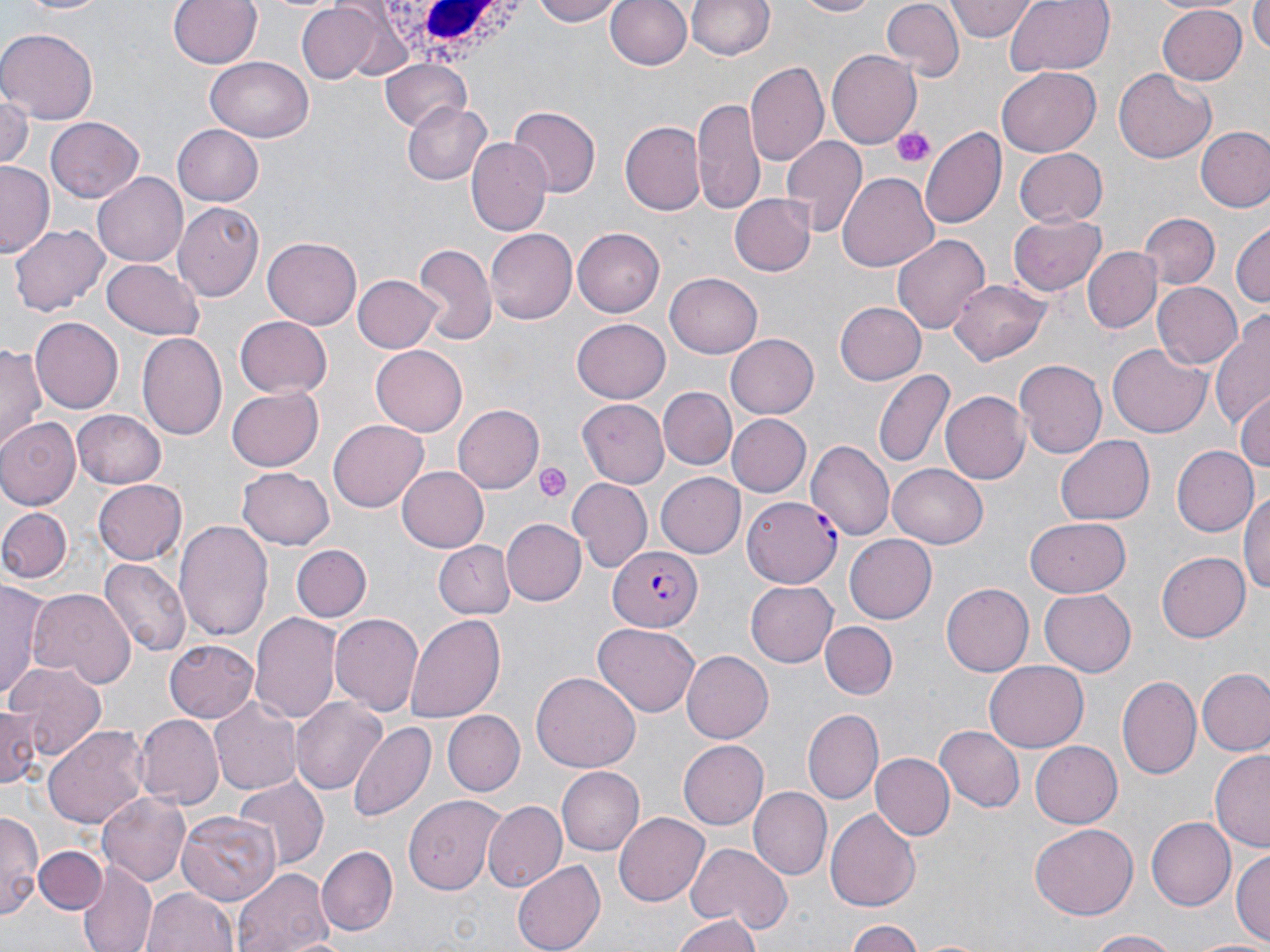
Approximate bounding boxes as (x1,y1)-(x2,y2) corner pairs in pixels. Platelet locations: (892,126)-(934,170), (534,462)-(571,502). White blood cell locations: (374,4)-(533,74). Uninfected red blood cell locations: (12,0)-(108,17), (168,0)-(261,70), (530,0)-(628,26), (606,0)-(691,72), (685,0)-(776,62), (793,0)-(881,18), (1003,0)-(1114,77), (1251,0)-(1270,54), (947,1)-(1037,41), (884,2)-(964,81), (294,3)-(394,84), (1155,3)-(1245,83), (0,27)-(98,122), (829,50)-(922,147), (205,55)-(314,143), (381,59)-(472,134), (747,61)-(828,167), (996,67)-(1101,156), (1114,68)-(1217,164), (0,90)-(33,172), (691,98)-(765,215), (403,103)-(490,184), (506,105)-(598,198), (46,118)-(144,204), (619,120)-(706,216), (170,122)-(266,210), (920,125)-(1005,229), (1196,126)-(1270,213), (468,137)-(553,235), (780,137)-(867,237), (1012,147)-(1107,229), (0,162)-(56,258), (836,171)-(938,274), (93,172)-(188,269), (728,194)-(816,277), (173,203)-(263,302), (1137,213)-(1220,290), (1009,215)-(1107,294), (1231,222)-(1269,310), (10,224)-(108,315), (486,228)-(577,326), (573,229)-(666,316), (892,232)-(990,335), (262,237)-(363,330), (412,244)-(496,348), (1084,248)-(1160,332), (101,257)-(204,339), (351,273)-(442,354), (665,273)-(763,358), (950,280)-(1052,364), (1152,282)-(1242,371), (835,300)-(926,386), (1211,311)-(1270,429), (234,315)-(332,397), (30,319)-(122,412), (572,320)-(670,402), (136,331)-(229,443), (724,334)-(818,418), (1107,343)-(1211,436), (0,345)-(45,456), (371,345)-(467,436), (1013,359)-(1105,460), (874,368)-(955,469), (660,386)-(736,468), (227,388)-(324,471), (942,392)-(1030,485), (1233,392)-(1270,477), (580,398)-(667,486), (454,405)-(544,492), (72,409)-(165,488), (726,413)-(811,497), (0,418)-(78,509), (328,420)-(429,512), (1056,436)-(1154,525), (807,439)-(894,541), (1171,443)-(1258,536), (888,463)-(989,548), (397,465)-(490,552), (235,467)-(336,551), (658,471)-(747,558), (568,476)-(651,571), (93,480)-(185,566), (1241,490)-(1270,599), (0,507)-(72,584), (1024,516)-(1132,595), (502,518)-(585,606), (174,519)-(275,640), (844,533)-(937,624), (432,540)-(512,620), (290,545)-(371,622), (1156,551)-(1250,642), (99,558)-(192,659), (0,579)-(51,704), (745,582)-(838,667), (941,582)-(1034,676), (28,588)-(135,689), (1039,588)-(1134,677), (251,611)-(341,723), (329,612)-(423,717), (406,613)-(504,723), (594,621)-(700,716), (821,621)-(897,700), (166,637)-(260,723), (680,651)-(771,744), (985,661)-(1087,750), (6,663)-(104,763), (1198,668)-(1270,756), (532,672)-(641,775), (1117,675)-(1201,779), (210,694)-(300,793), (292,697)-(384,794), (3,704)-(42,789), (804,709)-(884,803), (441,710)-(524,797), (135,714)-(223,808), (347,720)-(436,825), (43,724)-(154,829), (935,725)-(1025,813), (679,739)-(768,829), (1029,741)-(1121,828), (1210,750)-(1270,853), (870,754)-(954,841), (558,767)-(643,854), (232,775)-(326,873), (748,787)-(831,880), (99,792)-(190,884), (404,796)-(505,895), (485,801)-(567,894), (176,810)-(282,904), (826,811)-(920,909), (0,812)-(41,922), (615,812)-(708,905), (1148,815)-(1237,911), (1028,824)-(1138,919), (684,840)-(793,934), (34,845)-(108,915), (317,846)-(398,936), (1233,849)-(1269,949), (512,859)-(607,952), (76,864)-(159,952), (233,867)-(334,952), (142,886)-(240,952), (672,914)-(762,952), (844,919)-(923,951), (1083,929)-(1185,951), (1188,938)-(1270,952). Plasmodium falciparum-infected red blood cell locations: (741,495)-(841,590), (608,545)-(703,633). Slide-level diagnosis: Plasmodium falciparum. Thin blood film. Optical microscopy. 1000x magnification. Image is 1270×952 pixels. May-Grünwald-Giemsa stain. One field of a larger specimen.